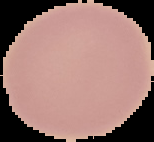
Summary:
  - Malaria status: uninfected
  - Image type: cell region segmented out of the field of view; surrounding area masked to black
  - Preparation: thin blood film
  - Image size: 154×142 pixels